Identify the blood parasite species.
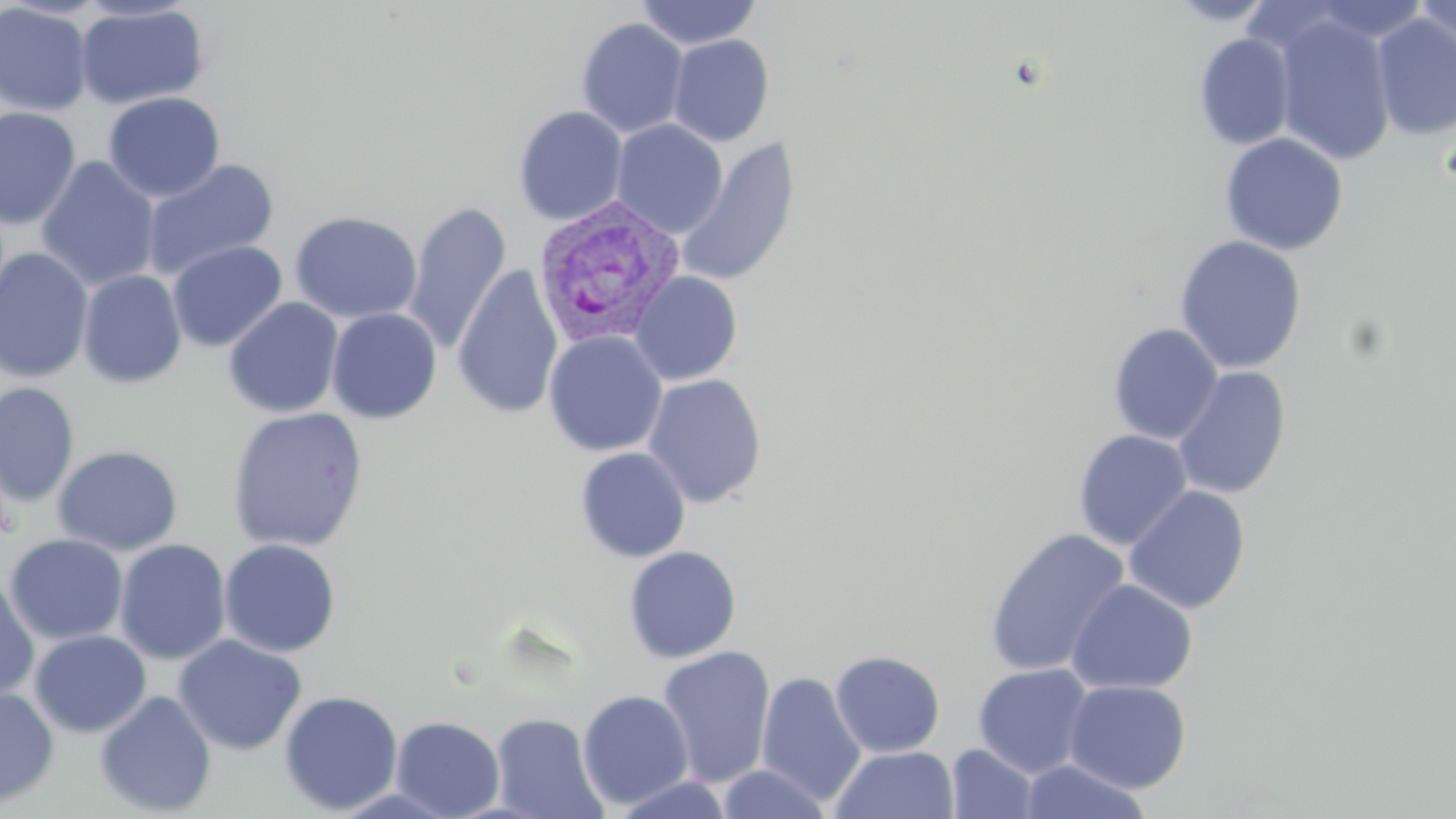
Plasmodium vivax.

image size = 1456×819 pixels
preparation = thin blood smear
field of view = single
modality = light microscopy
magnification = 1000x
Plasmodium vivax-infected red blood cell locations = approximate bounding boxes as [x1, y1, x2, y2] in pixels: [532, 196, 686, 350]
uninfected red blood cell locations = approximate bounding boxes as [x1, y1, x2, y2] in pixels: [634, 0, 763, 50], [1414, 0, 1455, 60], [0, 3, 94, 118], [74, 3, 210, 111], [1269, 11, 1397, 166], [1370, 12, 1456, 142], [575, 18, 690, 138], [1194, 33, 1296, 150], [667, 35, 775, 147], [103, 92, 225, 203], [513, 105, 628, 226], [0, 106, 82, 230], [611, 119, 727, 237], [1220, 132, 1349, 256], [676, 135, 801, 287], [36, 156, 161, 291], [141, 159, 280, 280], [403, 201, 511, 355], [289, 211, 422, 324], [1174, 235, 1307, 375], [167, 240, 287, 352], [0, 247, 94, 383], [452, 264, 564, 420], [77, 269, 187, 389], [629, 271, 743, 386], [223, 297, 344, 418], [326, 307, 442, 424], [1107, 323, 1223, 445], [543, 331, 667, 456], [1172, 367, 1291, 499], [643, 373, 767, 508], [0, 382, 80, 507], [226, 406, 369, 552], [1073, 430, 1193, 550], [52, 444, 183, 555], [574, 446, 691, 562], [1124, 486, 1251, 614], [984, 527, 1130, 677], [3, 533, 129, 646], [219, 538, 341, 657], [113, 539, 231, 665], [623, 545, 741, 664], [0, 575, 40, 703], [1066, 579, 1198, 695], [29, 630, 151, 737], [173, 634, 307, 756], [655, 645, 777, 788], [830, 650, 946, 757], [972, 663, 1095, 777], [756, 671, 867, 807], [1064, 680, 1191, 792], [0, 685, 59, 809], [576, 689, 694, 810], [94, 690, 217, 817], [278, 690, 404, 815], [491, 712, 607, 819], [390, 715, 505, 818], [945, 743, 1041, 819], [830, 745, 959, 819], [1017, 758, 1154, 818], [716, 764, 834, 818], [608, 773, 736, 819]
stain = May-Grünwald-Giemsa